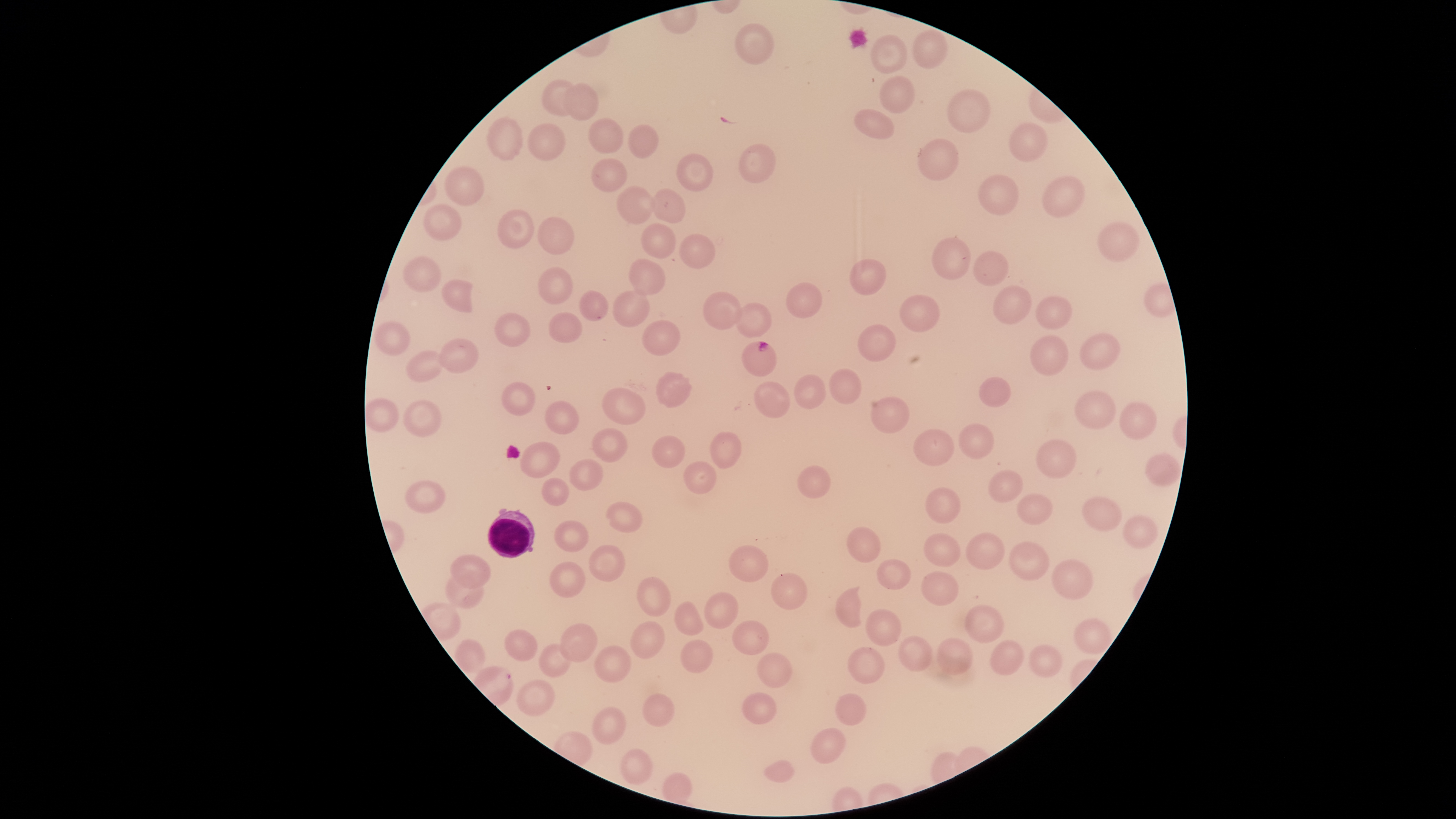
Approximate bounding boxes as (left, top, right, bottom) in pixels. Parasitized RBCs: (741, 341, 777, 376). WBCs: (488, 508, 535, 559). Uninfected RBCs: (734, 23, 774, 65), (912, 29, 948, 69), (870, 35, 907, 73), (880, 75, 915, 114), (541, 80, 576, 116), (562, 83, 598, 121), (947, 89, 991, 133), (853, 109, 894, 139), (487, 117, 524, 161), (588, 118, 624, 154), (1008, 122, 1048, 162), (528, 123, 565, 160), (628, 124, 659, 159), (917, 138, 959, 180), (738, 144, 776, 183), (676, 153, 713, 191), (591, 158, 628, 192), (444, 166, 484, 206), (978, 175, 1018, 215), (1042, 176, 1085, 218), (617, 186, 653, 224), (651, 188, 685, 224), (423, 204, 461, 240), (497, 208, 534, 248), (537, 216, 574, 255), (1098, 222, 1139, 262), (641, 223, 676, 258), (679, 234, 715, 269), (932, 237, 971, 280), (973, 251, 1009, 286), (403, 255, 441, 291), (628, 258, 665, 295), (850, 259, 886, 295), (538, 267, 573, 304), (442, 279, 473, 313), (785, 282, 822, 319), (993, 285, 1032, 324), (580, 290, 608, 321), (613, 290, 650, 328), (703, 292, 742, 331), (900, 295, 940, 332), (1035, 295, 1073, 330), (735, 302, 771, 338), (549, 312, 582, 343), (494, 313, 531, 347), (642, 320, 680, 357), (375, 321, 410, 356), (858, 325, 895, 361), (1080, 332, 1121, 370), (1030, 334, 1069, 376), (439, 338, 480, 373), (406, 350, 444, 381), (830, 368, 862, 404), (656, 372, 692, 408), (794, 374, 825, 409), (979, 376, 1011, 407), (501, 381, 535, 415), (754, 381, 790, 418), (602, 387, 646, 424), (1074, 389, 1116, 428), (872, 397, 909, 433), (366, 398, 399, 432), (402, 400, 442, 437), (545, 401, 578, 434), (1119, 402, 1156, 439), (959, 423, 994, 459), (592, 428, 627, 462), (913, 429, 954, 466), (710, 431, 741, 469), (652, 435, 685, 468), (1036, 439, 1077, 478), (520, 441, 560, 478), (1145, 453, 1181, 486), (569, 459, 602, 490), (684, 461, 717, 494), (797, 465, 831, 499), (989, 470, 1023, 503), (541, 478, 569, 506), (405, 480, 446, 513), (926, 487, 961, 523), (1017, 493, 1053, 525), (1081, 496, 1122, 531), (606, 502, 642, 533), (1123, 515, 1158, 549), (554, 520, 588, 552), (846, 526, 881, 563), (965, 531, 1005, 570), (924, 533, 961, 567), (1009, 541, 1049, 580), (589, 545, 625, 582), (728, 545, 769, 582), (450, 554, 491, 588), (877, 559, 911, 590), (1051, 559, 1094, 600), (549, 562, 585, 598), (921, 571, 958, 605), (770, 573, 808, 610), (445, 575, 484, 608), (637, 577, 671, 616), (834, 586, 863, 628), (704, 592, 739, 629), (674, 601, 703, 636), (965, 604, 1004, 643), (865, 608, 901, 646), (1074, 618, 1113, 654), (732, 620, 769, 655), (630, 621, 665, 659), (560, 623, 597, 662), (504, 629, 538, 661), (898, 635, 932, 672), (937, 637, 973, 675), (453, 638, 486, 673), (680, 639, 713, 673), (990, 639, 1024, 675), (538, 644, 571, 677), (1028, 644, 1062, 678), (594, 645, 632, 682), (848, 646, 885, 684), (757, 652, 792, 688), (516, 679, 556, 716), (742, 692, 777, 724), (642, 693, 675, 727), (835, 693, 866, 725), (592, 706, 626, 744), (810, 727, 846, 763), (620, 748, 653, 785), (764, 759, 795, 783), (662, 772, 692, 803). The visible region is circular. Presence: malaria parasites identified. Species: Plasmodium falciparum. Thin smear of blood. Photographed with a smartphone camera through the microscope eyepiece. Image is 1456×819 pixels. Giemsa stain. One field of view of the specimen.